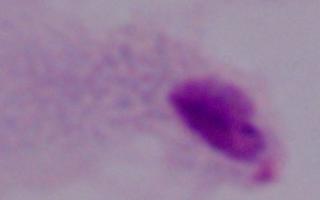 A trichomonad is shown. 1000x magnification. Micrograph.